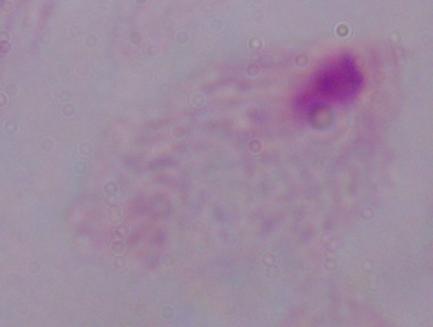 A trichomonad is shown. Captured at 1000x magnification. Micrograph.